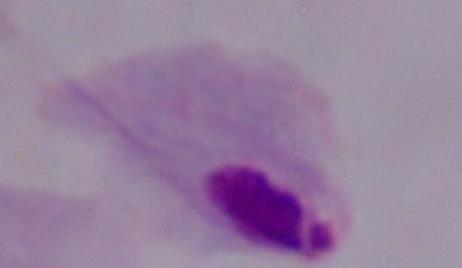
A trichomonad is shown. 1000x magnification. Photomicrograph.